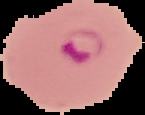
Summary:
  - Image type: segmented cell region with the area outside set to black
  - Image size: 145×115 pixels
  - Result: Plasmodium parasites detected
  - Preparation: thin blood smear